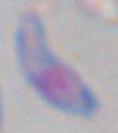

Summary:
  - Magnification: 1000x
  - Modality: photomicrograph
  - Identification: Toxoplasma gondii